Name the parasite shown.
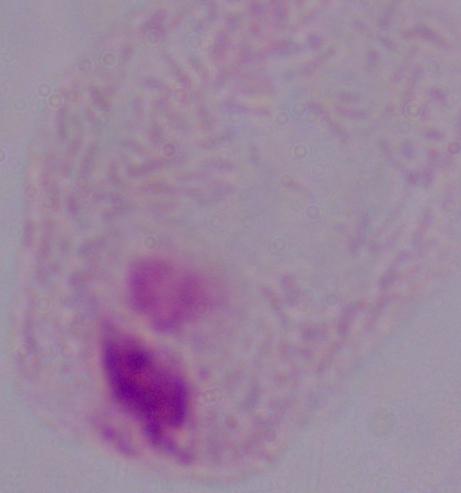

A trichomonad.

1000x magnification. Photomicrograph.